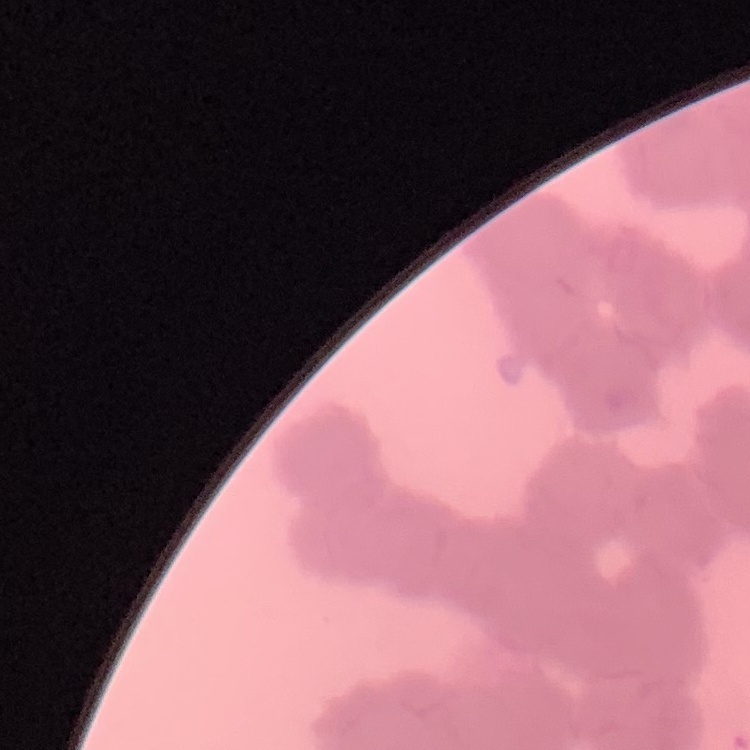

Summary:
  - Erythrocyte morphology: rouleaux formation
  - Preparation: thin blood smear
  - Stain: Field's or Giemsa
  - Image type: square crop of a larger photomicrograph